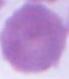
Summary:
  - Identification: erythrocyte
  - Modality: micrograph
  - Magnification: 1000x